Locate every blood parasite and identify its species.
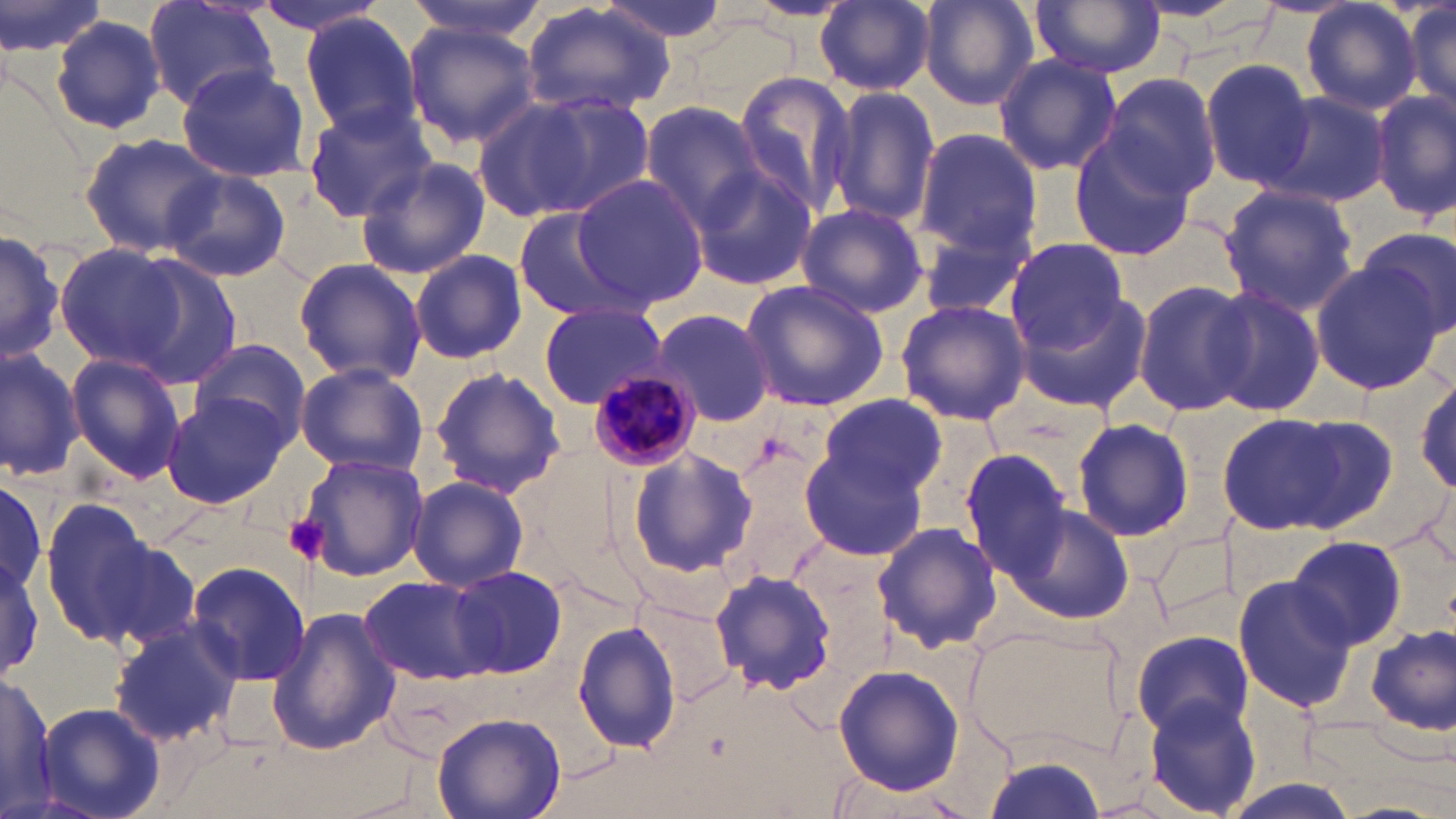
Approximate bounding boxes as (x1, y1, x2, y2) in pixels.
Plasmodium malariae-infected red blood cells: (586, 369, 701, 471).
No Plasmodium falciparum, Plasmodium ovale, Plasmodium vivax, Babesia divergens, or Trypanosoma brucei observed.

slide_level_diagnosis: Plasmodium malariae
field_of_view: one of a larger specimen
modality: light microscopy
stain: May-Grünwald-Giemsa
uninfected_red_blood_cell_locations: 'approximate bounding boxes as (x1, y1, x2, y2) in pixels: (0, 0, 109, 68), (248, 0, 394, 37), (405, 0, 553, 44), (595, 0, 734, 45), (918, 0, 1041, 111), (1031, 0, 1167, 78), (1301, 0, 1423, 117), (1404, 0, 1456, 122), (144, 1, 280, 113), (814, 1, 937, 95), (521, 4, 673, 119), (299, 12, 421, 138), (50, 15, 168, 135), (402, 22, 541, 150), (992, 51, 1122, 179), (1199, 59, 1318, 188), (177, 63, 312, 185), (730, 71, 858, 222), (1096, 73, 1221, 203), (825, 85, 940, 227), (1372, 89, 1456, 220), (512, 91, 657, 216), (1260, 91, 1394, 210), (469, 96, 602, 223), (636, 100, 767, 233), (301, 103, 438, 221), (913, 129, 1042, 259), (79, 131, 229, 256), (1068, 134, 1198, 263), (355, 156, 492, 277), (690, 164, 816, 291), (162, 167, 293, 284), (570, 173, 707, 312), (1219, 185, 1359, 317), (795, 204, 928, 316), (513, 208, 630, 320), (917, 225, 1033, 320), (1356, 225, 1455, 343), (773, 227, 913, 391), (0, 229, 66, 366), (1004, 237, 1129, 354), (54, 243, 190, 369), (411, 250, 527, 364), (125, 254, 246, 390), (293, 257, 428, 387), (1310, 260, 1442, 394), (1131, 279, 1253, 416), (738, 280, 889, 412), (1016, 285, 1154, 415), (1203, 287, 1324, 419), (895, 299, 1031, 427), (538, 302, 664, 408), (650, 308, 776, 427), (189, 338, 310, 449), (0, 343, 85, 481), (66, 352, 187, 484), (295, 362, 429, 478), (427, 365, 565, 499), (1412, 370, 1456, 495), (817, 392, 947, 499), (160, 393, 289, 508), (1217, 412, 1354, 535), (1279, 415, 1401, 532), (1072, 418, 1194, 541), (801, 441, 930, 559), (727, 444, 832, 579), (627, 447, 758, 578), (958, 449, 1072, 577), (293, 452, 427, 581), (1, 471, 45, 601), (407, 476, 529, 592), (38, 503, 163, 653), (1002, 503, 1133, 624), (871, 521, 1002, 652), (81, 526, 206, 650), (1288, 537, 1409, 649), (0, 549, 45, 676), (184, 560, 311, 687), (450, 565, 565, 677), (711, 566, 841, 694), (1233, 570, 1361, 715), (357, 575, 496, 684), (628, 590, 738, 708), (267, 605, 402, 757), (108, 617, 242, 749), (573, 621, 684, 757), (962, 622, 1128, 763), (1365, 623, 1454, 736), (1133, 631, 1252, 737), (833, 663, 962, 795), (0, 672, 58, 814), (1140, 694, 1264, 817), (35, 702, 163, 819), (433, 711, 565, 819), (985, 745, 1110, 819)'
preparation: thin blood film
image_size: 1456×819 pixels
platelet_locations: 'approximate bounding boxes as (x1, y1, x2, y2) in pixels: (281, 516, 328, 566)'
magnification: 1000x